Describe the morphology of the red blood cells.
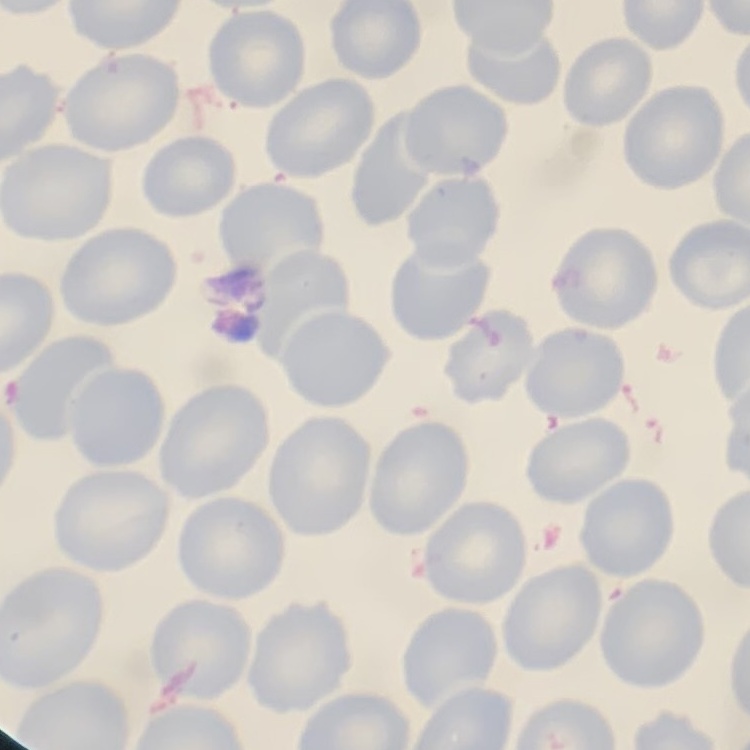

They show no rouleaux formation.

Summary:
  - Stain: Field's or Giemsa
  - Image type: one tile cut from a larger photomicrograph
  - Preparation: thin peripheral smear